Locate every uninfected red blood cell.
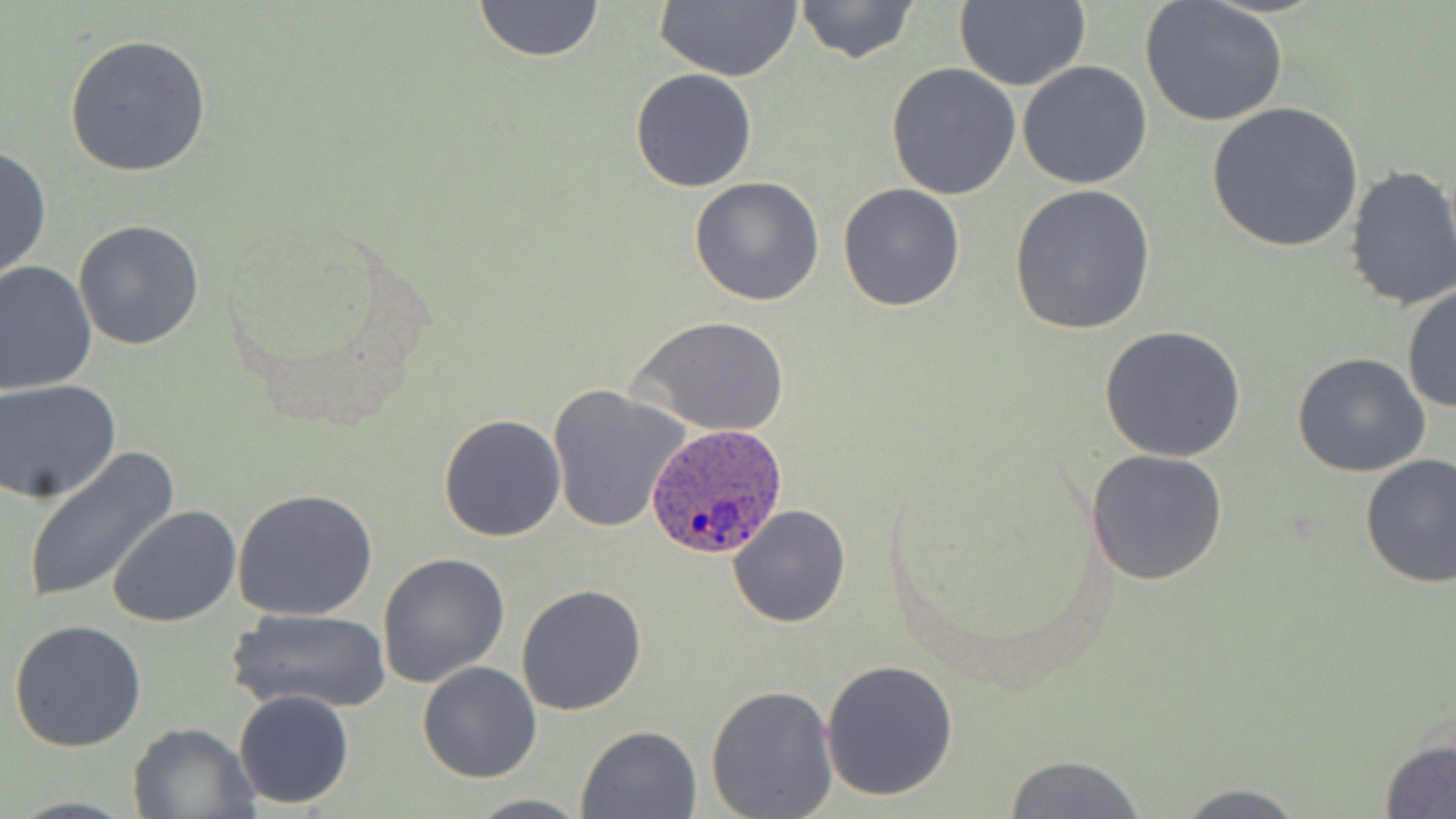
Approximate bounding boxes as (x1, y1, x2, y2) in pixels.
Uninfected red blood cells: (474, 0, 604, 64), (653, 0, 802, 82), (795, 0, 921, 65), (953, 0, 1090, 91), (1139, 1, 1288, 127), (63, 33, 211, 178), (1017, 61, 1152, 189), (886, 64, 1020, 200), (630, 68, 758, 193), (1205, 102, 1364, 253), (0, 145, 51, 284), (1341, 163, 1456, 312), (689, 176, 824, 305), (1008, 183, 1156, 335), (838, 184, 966, 312), (73, 220, 205, 352), (0, 259, 98, 395), (1404, 283, 1456, 417), (632, 316, 790, 438), (1098, 326, 1248, 465), (1292, 352, 1432, 479), (1, 379, 122, 504), (548, 385, 690, 534), (438, 413, 566, 542), (1083, 447, 1229, 585), (22, 449, 179, 604), (1358, 453, 1456, 589), (232, 489, 377, 621), (728, 504, 851, 628), (108, 505, 241, 628), (377, 553, 511, 689), (516, 584, 648, 717), (226, 608, 391, 713), (7, 620, 147, 753), (821, 660, 959, 801), (417, 662, 541, 783), (705, 682, 839, 818), (233, 689, 355, 810), (127, 722, 259, 818), (576, 725, 701, 818), (1380, 737, 1456, 819), (1001, 754, 1148, 819), (1167, 782, 1314, 819), (462, 793, 591, 818).

Summary:
  - Plasmodium ovale-infected red blood cell locations: (646, 422, 790, 561)
  - Slide-level diagnosis: Plasmodium ovale
  - Image size: 1456×819 pixels
  - Preparation: thin blood film
  - Magnification: 1000x
  - Field of view: single
  - Stain: May-Grünwald-Giemsa
  - Modality: light microscopy